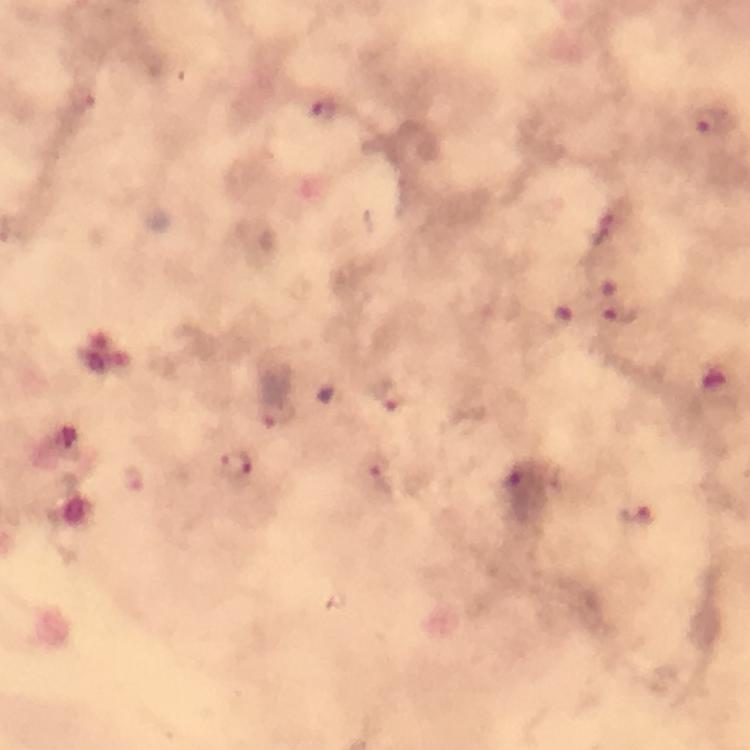

preparation = thick blood film
magnification = 100x
malaria parasite locations = approximate centers as {x, y} in pixels: {81, 97}, {324, 111}, {712, 121}, {601, 229}, {621, 313}, {390, 396}, {277, 416}, {375, 464}, {236, 465}, {636, 514}
context = from a malaria diagnostic workup
stain = Giemsa
cropped from = a single field of view
capture = smartphone camera through the microscope
image size = 750×750 pixels
immersion oil = applied